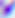
identification: Toxoplasma gondii
modality: photomicrograph
magnification: 400x